Comment on the morphology of the erythrocytes.
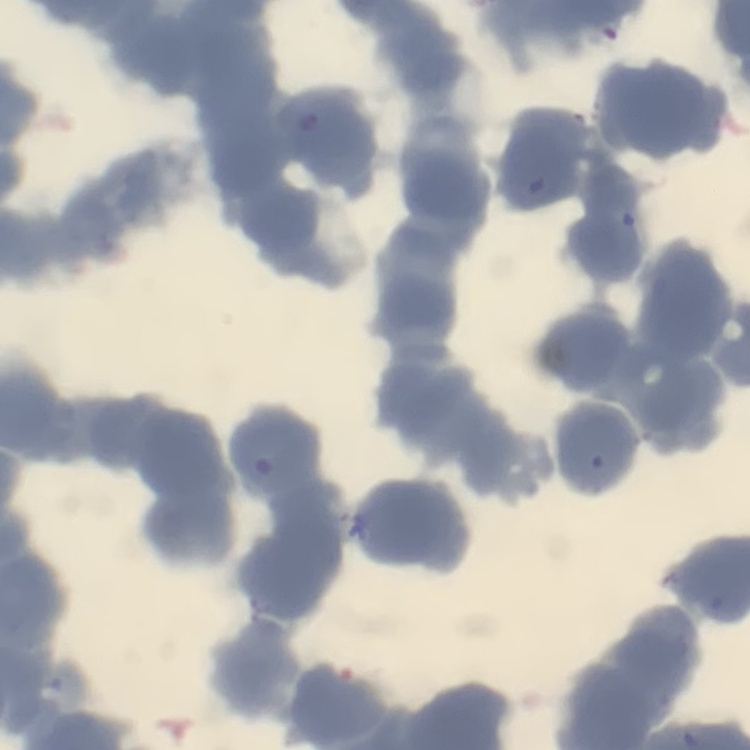

Rouleaux formation.

preparation = thin blood smear
image type = square crop of a larger photomicrograph
stain = Field's or Giemsa